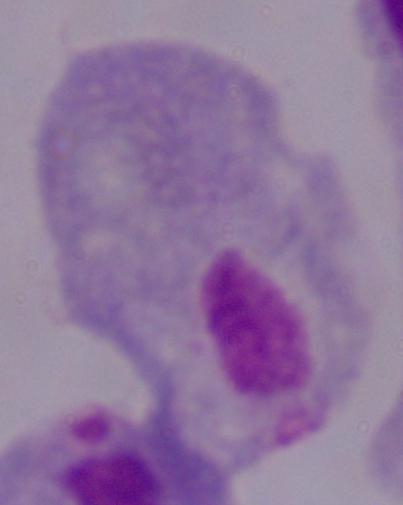

identification = trichomonad
magnification = 1000x
modality = micrograph